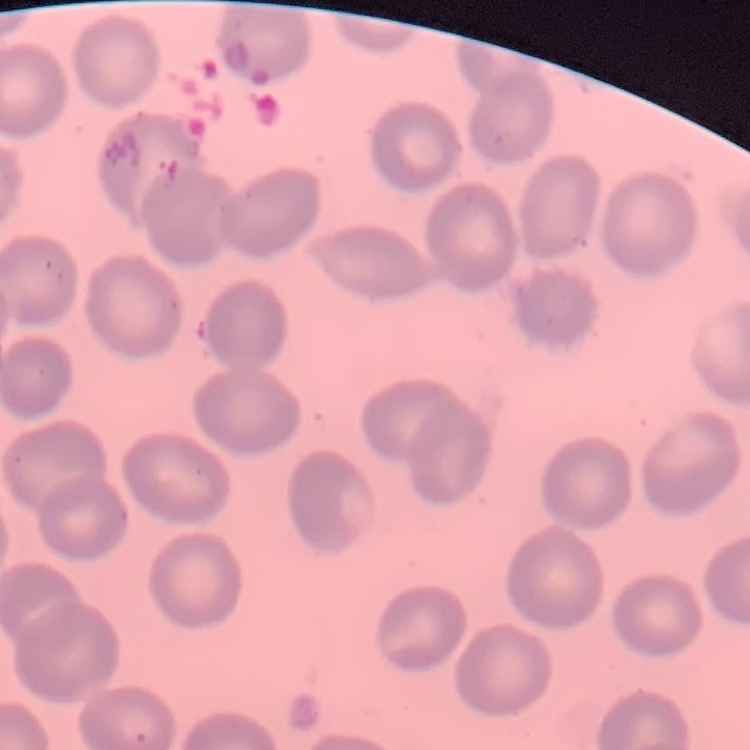
The red blood cells exhibit no rouleaux formation. Thin blood smear. One tile cut from a larger photomicrograph. Stained with either Field's or Giemsa.